Identify the parasite.
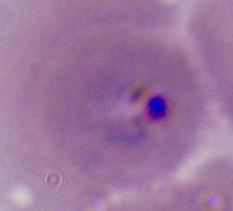

Plasmodium.

Photomicrograph. Captured at either 400x or 1000x magnification.